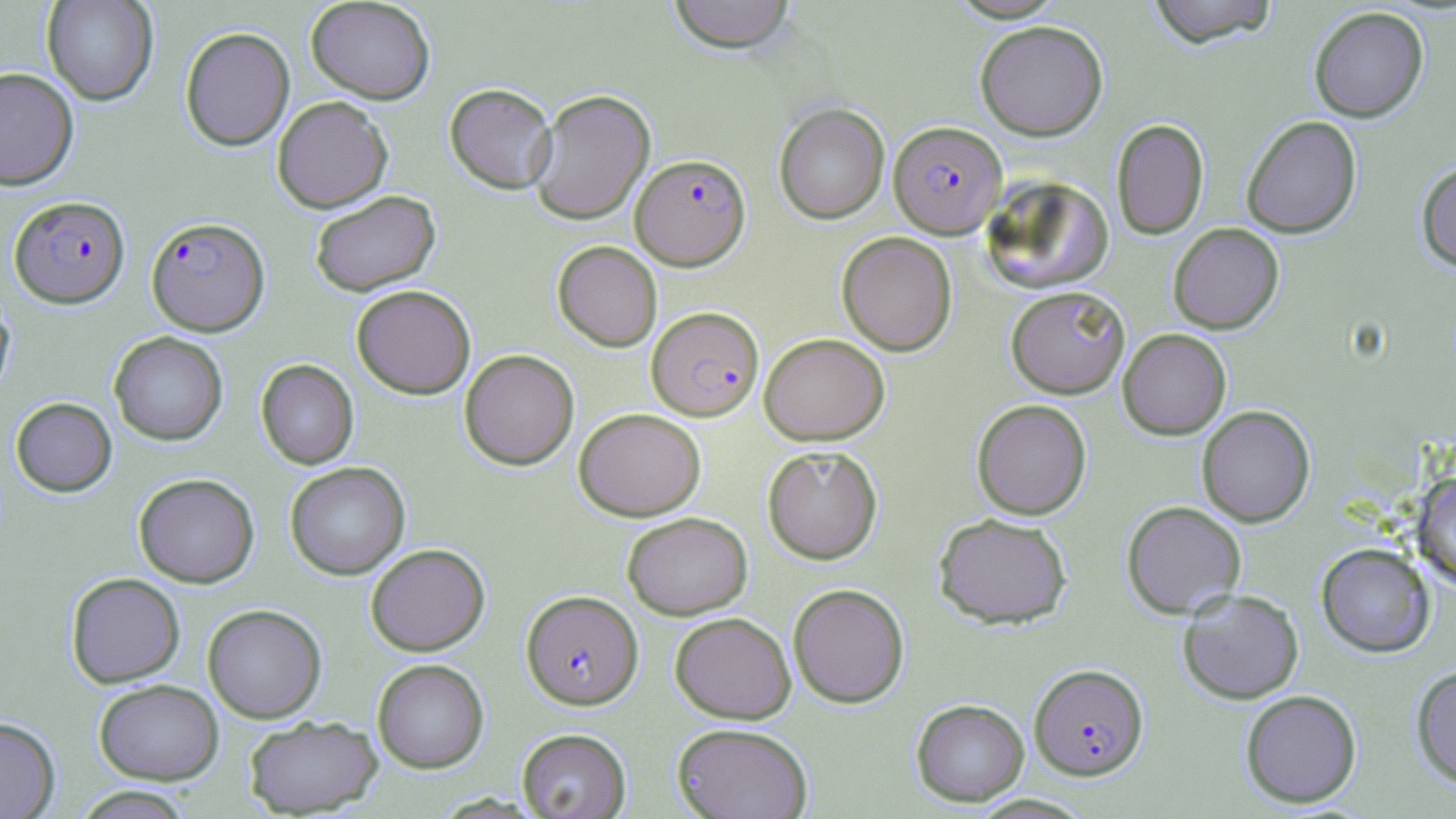
slide-level diagnosis = Plasmodium falciparum
magnification = 1000x
stain = May-Grünwald-Giemsa
uninfected red blood cell locations = approximate bounding boxes as (x1,y1)-(x2,y2) corner pairs in pixels: (41,0)-(159,105), (305,0)-(436,104), (668,0)-(796,53), (1146,0)-(1279,47), (1309,6)-(1429,122), (975,20)-(1108,140), (180,26)-(295,151), (0,67)-(79,190), (444,83)-(557,193), (529,89)-(655,225), (272,96)-(393,213), (774,102)-(890,224), (1241,115)-(1362,238), (1111,118)-(1209,240), (1416,160)-(1456,273), (981,176)-(1114,294), (309,190)-(441,297), (1169,223)-(1284,334), (837,231)-(958,355), (552,240)-(662,351), (351,284)-(476,399), (1006,286)-(1130,398), (0,293)-(15,405), (1118,328)-(1231,439), (109,331)-(228,445), (759,332)-(889,445), (459,349)-(579,470), (256,359)-(359,469), (10,397)-(117,496), (972,399)-(1092,519), (1197,405)-(1315,527), (573,407)-(706,521), (762,444)-(883,564), (284,461)-(411,580), (1412,472)-(1456,589), (133,473)-(259,587), (1121,500)-(1246,618), (622,512)-(753,620), (933,513)-(1073,629), (1316,542)-(1435,657), (365,543)-(490,656), (66,572)-(185,688), (788,583)-(910,708), (1178,588)-(1304,704), (202,604)-(327,723), (670,612)-(796,724), (372,659)-(489,773), (1411,664)-(1456,789), (94,679)-(224,785), (1240,689)-(1362,808), (911,698)-(1029,806), (0,716)-(60,819), (243,716)-(383,817), (672,722)-(814,819), (517,728)-(631,819), (70,786)-(196,818)
modality = optical microscopy
image size = 1456×819 pixels
preparation = thin blood smear
field of view = single
Plasmodium falciparum-infected red blood cell locations = approximate bounding boxes as (x1,y1)-(x2,y2) corner pairs in pixels: (889,120)-(1007,237), (631,153)-(751,270), (10,195)-(130,308), (146,216)-(270,336), (646,306)-(764,421), (521,590)-(643,710), (1029,663)-(1148,780)